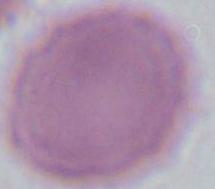

Summary:
  - Identification: red blood cell
  - Magnification: 1000x
  - Modality: micrograph